State which cell type is depicted.
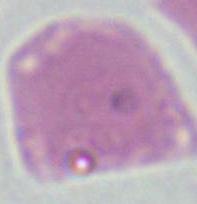
An erythrocyte.

Micrograph. Captured at 1000x magnification.